Assess this cell for malaria.
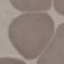
It is uninfected.

{
  "capture": "smartphone through the microscope eyepiece",
  "stain": "Giemsa",
  "preparation": "thin blood smear",
  "image_type": "automatically extracted cell patch, resized to 64 × 64 pixels"
}